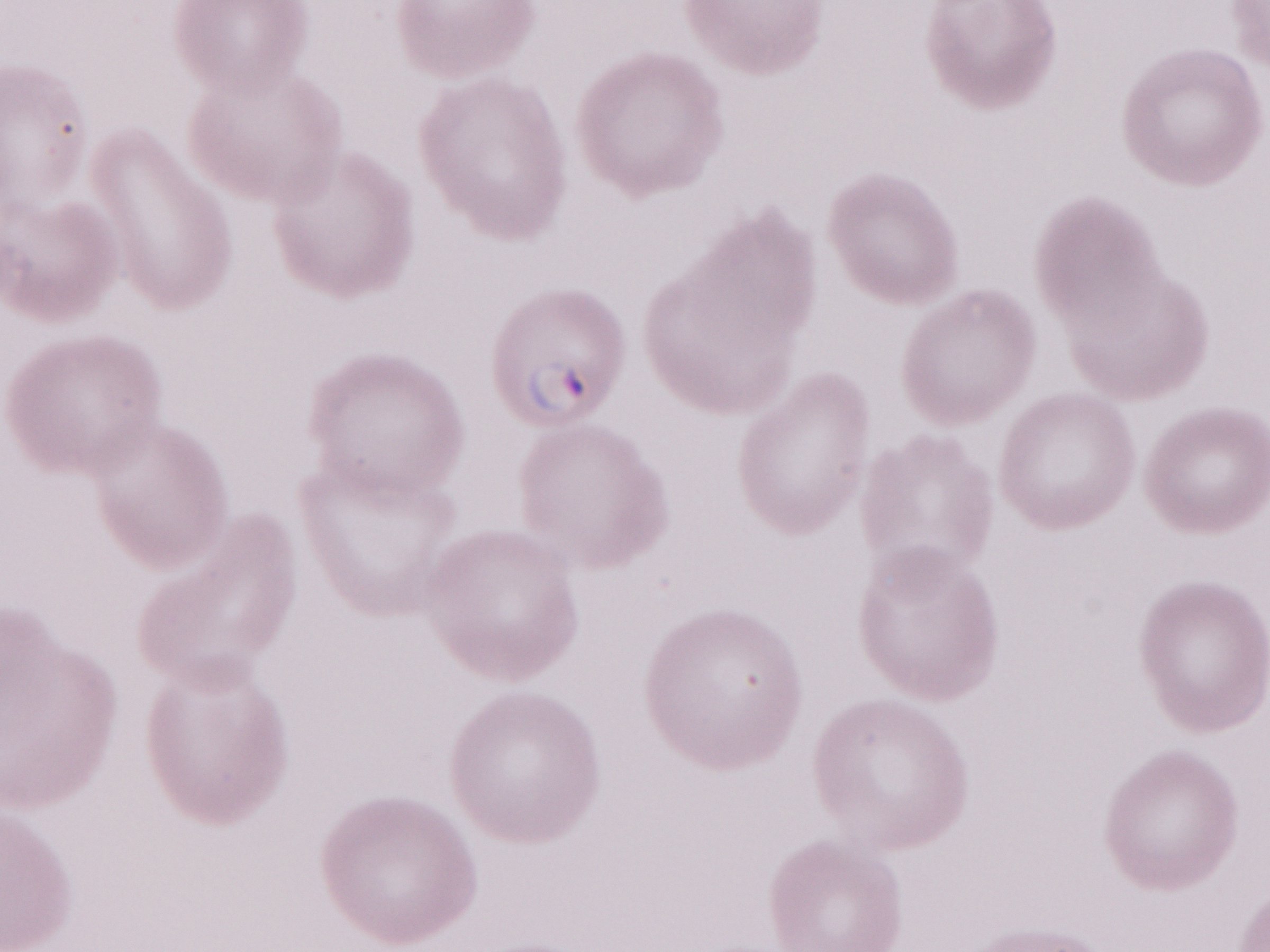

Malaria diagnosis (patient-level): positive. Thin peripheral-blood smear. 1,000x magnification. May-Grünwald-Giemsa-stained preparation. Single field of view. Image is 1270×952 pixels. Olympus BX43 microscope, Olympus DP73 camera.